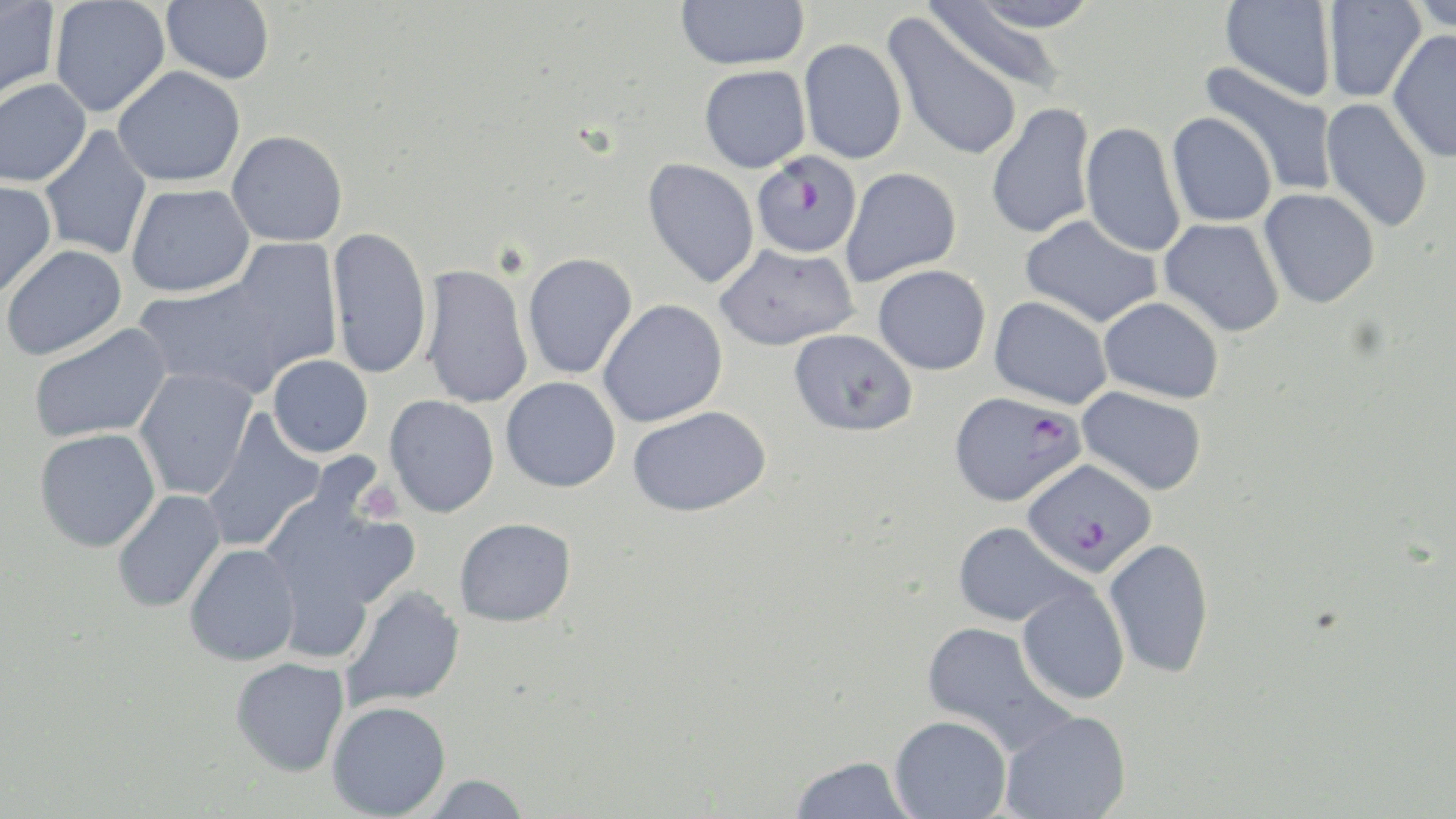

Summary:
  - Coordinate format: approximate bounding boxes as (x1,y1)-(x2,y2) corner pairs in pixels
  - Uninfected red blood cell locations: (48,0)-(171,118), (161,0)-(275,84), (675,0)-(809,70), (956,0)-(1102,33), (1220,0)-(1336,102), (1322,1)-(1426,103), (1409,1)-(1456,36), (0,2)-(61,105), (923,3)-(1074,95), (882,13)-(1024,162), (1388,29)-(1456,163), (798,38)-(907,164), (1200,60)-(1338,196), (699,65)-(811,172), (112,66)-(245,188), (0,79)-(92,187), (1320,98)-(1433,233), (986,102)-(1096,240), (1166,112)-(1277,228), (1080,121)-(1186,259), (38,126)-(152,260), (226,130)-(348,247), (643,158)-(760,289), (840,167)-(961,286), (0,180)-(56,301), (126,184)-(255,298), (1259,188)-(1380,308), (1019,214)-(1162,329), (1159,218)-(1285,337), (326,226)-(433,379), (226,238)-(343,378), (714,243)-(859,351), (1,244)-(126,360), (522,252)-(638,380), (419,264)-(533,410), (873,264)-(991,375), (132,273)-(294,397), (989,296)-(1113,409), (1097,296)-(1224,403), (598,299)-(728,427), (28,323)-(172,443), (789,328)-(918,436), (267,354)-(373,457), (134,367)-(258,500), (501,376)-(621,492), (1076,387)-(1207,495), (384,395)-(499,517), (627,405)-(772,517), (200,410)-(327,552), (34,428)-(161,552), (111,489)-(226,612), (259,495)-(416,657), (455,517)-(576,627), (953,521)-(1086,627), (1104,537)-(1215,679), (184,543)-(301,666), (1017,584)-(1130,705), (340,585)-(465,710), (921,620)-(1072,754), (230,657)-(350,776), (327,700)-(451,819), (1000,709)-(1132,819), (890,715)-(1012,818), (789,755)-(917,818), (420,774)-(531,818)
  - Plasmodium falciparum-infected red blood cell locations: (752,151)-(862,258), (949,391)-(1086,508), (1021,459)-(1157,577)
  - Platelet locations: (355,481)-(404,526)
  - Slide-level diagnosis: Plasmodium falciparum
  - Modality: optical microscopy
  - Preparation: thin blood smear
  - Magnification: 1000x
  - Image size: 1456×819 pixels
  - Stain: May-Grünwald-Giemsa
  - Field of view: one of a larger specimen